Give the extent of all Plasmodium malariae-infected red blood cells.
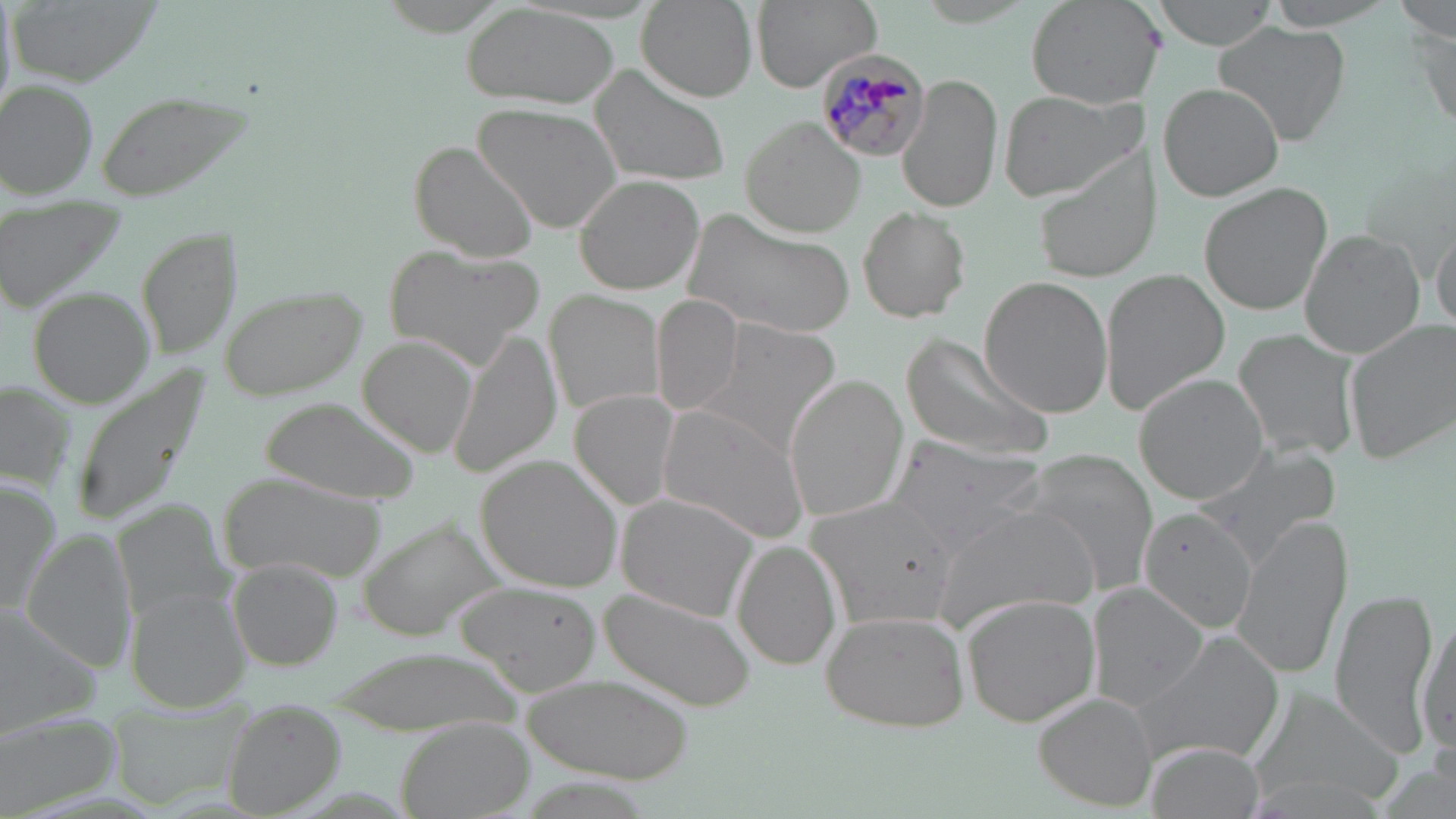
Approximate bounding boxes as [x1, y1, x2, y2] in pixels.
Plasmodium malariae-infected red blood cells: [816, 51, 929, 163].

Uninfected red blood cell locations: [750, 0, 881, 90], [1023, 0, 1158, 111], [1150, 0, 1279, 50], [1264, 0, 1406, 29], [1392, 0, 1456, 43], [635, 1, 756, 104], [463, 3, 620, 112], [1406, 19, 1455, 132], [1212, 21, 1353, 146], [592, 66, 733, 187], [899, 70, 1002, 214], [1, 79, 96, 198], [1159, 82, 1285, 202], [1000, 90, 1139, 199], [95, 91, 255, 201], [474, 105, 624, 233], [741, 117, 866, 238], [411, 141, 541, 263], [1035, 154, 1156, 283], [575, 176, 704, 295], [1197, 182, 1332, 317], [856, 205, 973, 324], [680, 209, 851, 338], [1430, 221, 1455, 340], [139, 227, 239, 360], [1298, 227, 1426, 359], [391, 246, 537, 368], [1098, 267, 1228, 413], [978, 278, 1112, 417], [221, 285, 369, 400], [27, 289, 156, 407], [549, 291, 669, 415], [652, 296, 745, 416], [701, 318, 843, 457], [1343, 318, 1456, 464], [1232, 327, 1361, 462], [449, 332, 561, 476], [897, 334, 1051, 464], [360, 337, 481, 459], [66, 360, 216, 532], [784, 374, 909, 522], [1134, 374, 1270, 505], [0, 381, 75, 488], [571, 389, 681, 510], [264, 401, 418, 502], [659, 403, 812, 544], [884, 437, 1045, 551], [1188, 440, 1341, 567], [1012, 449, 1159, 594], [479, 457, 625, 591], [223, 475, 383, 581], [0, 484, 60, 613], [618, 494, 760, 622], [809, 497, 960, 627], [116, 501, 233, 619], [932, 504, 1099, 631], [1137, 506, 1259, 633], [1232, 511, 1352, 679], [26, 534, 136, 673], [734, 539, 843, 670], [226, 559, 340, 670], [457, 583, 601, 691], [1088, 583, 1211, 711], [1329, 587, 1441, 757], [600, 589, 754, 710], [129, 590, 252, 711], [961, 592, 1100, 726], [0, 607, 103, 730], [1414, 607, 1453, 759], [820, 612, 971, 733], [1130, 630, 1285, 769], [521, 678, 692, 781], [1247, 688, 1402, 808], [1035, 692, 1161, 809], [218, 701, 343, 817], [0, 715, 122, 813], [399, 718, 536, 819], [1144, 741, 1265, 819], [1243, 770, 1394, 817]. Slide-level diagnosis: Plasmodium malariae. 1000x magnification. Image is 1456×819 pixels. Thin blood smear. Optical microscopy. Single field of view. May-Grünwald-Giemsa-stained preparation.